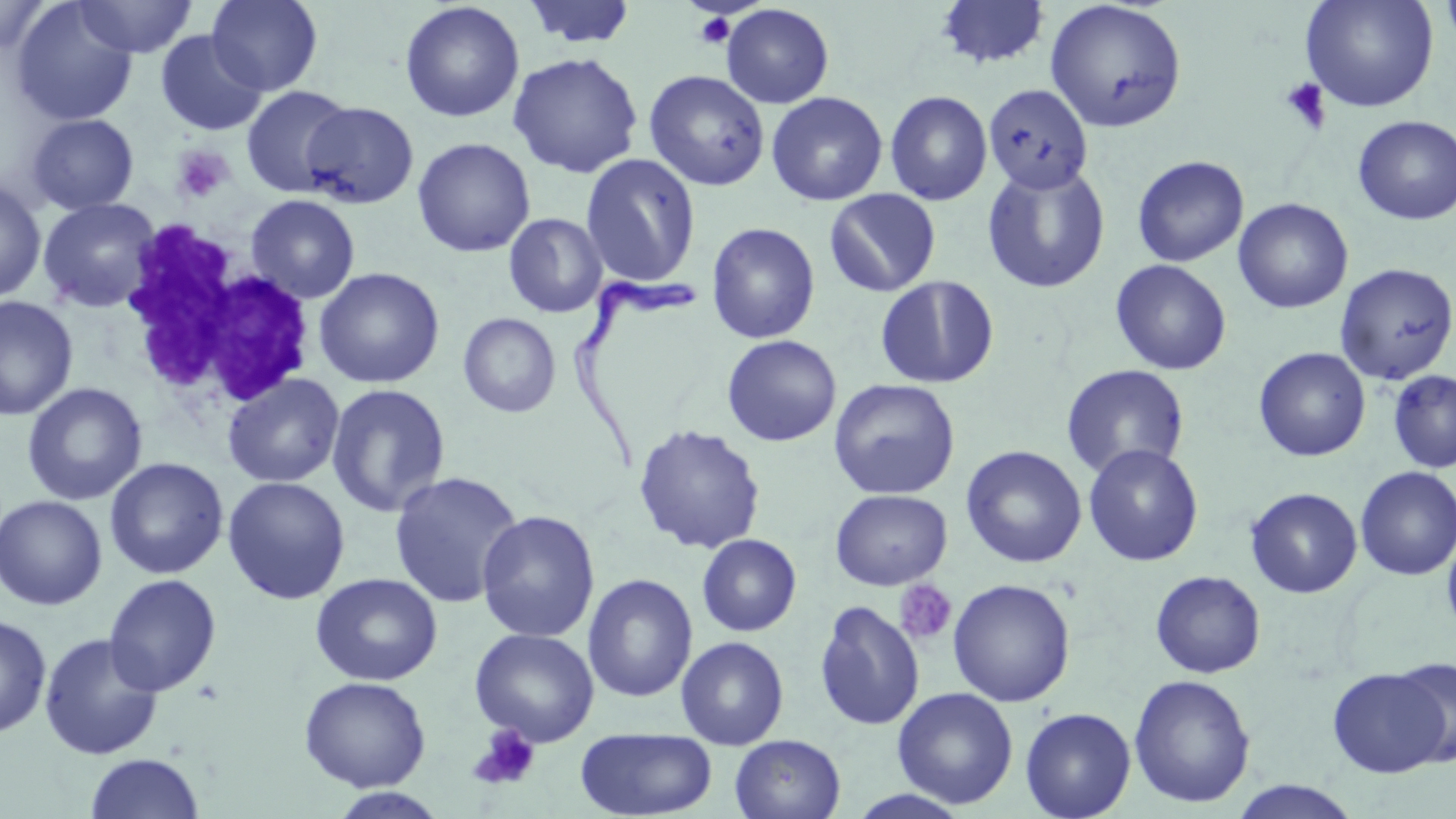
slide_level_diagnosis: Trypanosoma brucei
platelet_locations: 'approximate bounding boxes as (x1,y1)-(x2,y2) corner pairs in pixels: (692,12)-(735,51), (1280,77)-(1332,133), (171,144)-(234,205), (894,580)-(958,646), (469,724)-(541,791)'
white_blood_cell_locations: 'approximate bounding boxes as (x1,y1)-(x2,y2) corner pairs in pixels: (113,226)-(320,416)'
magnification: 1000x
preparation: thin blood film
stain: May-Grünwald-Giemsa
field_of_view: single
trypanosoma_brucei_locations: 'approximate bounding boxes as (x1,y1)-(x2,y2) corner pairs in pixels: (569,261)-(705,470)'
image_size: 1456×819 pixels
modality: light microscopy
uninfected_red_blood_cell_locations: 'approximate bounding boxes as (x1,y1)-(x2,y2) corner pairs in pixels: (72,0)-(198,58), (206,0)-(324,95), (523,0)-(637,49), (934,0)-(1051,70), (1300,0)-(1439,113), (1439,0)-(1456,52), (1,1)-(55,53), (1045,1)-(1188,133), (399,2)-(525,123), (11,3)-(138,126), (719,4)-(834,109), (155,30)-(268,136), (508,52)-(644,178), (644,70)-(770,191), (983,83)-(1094,194), (240,85)-(354,197), (884,90)-(993,206), (765,91)-(888,206), (300,101)-(419,209), (26,114)-(140,215), (1353,116)-(1456,225), (412,137)-(536,257), (580,154)-(701,289), (1133,155)-(1248,267), (981,163)-(1111,294), (0,178)-(47,304), (824,189)-(941,297), (245,194)-(360,304), (38,197)-(162,314), (1233,198)-(1353,314), (503,213)-(608,318), (706,222)-(820,343), (1110,259)-(1231,375), (1334,263)-(1456,385), (313,267)-(445,389), (875,275)-(1000,389), (0,296)-(79,421), (458,313)-(561,418), (722,335)-(841,447), (1253,346)-(1371,462), (1061,364)-(1189,480), (1387,369)-(1456,473), (222,373)-(345,488), (828,378)-(961,500), (22,382)-(147,506), (325,383)-(451,517), (633,424)-(766,554), (1083,443)-(1203,566), (961,445)-(1087,568), (104,457)-(229,579), (1355,466)-(1456,580), (388,470)-(524,609), (222,476)-(350,604), (1245,487)-(1362,598), (830,489)-(952,590), (0,494)-(107,610), (477,510)-(600,642), (1441,526)-(1456,639), (696,533)-(802,637), (1150,570)-(1266,678), (310,572)-(443,686), (103,573)-(222,697), (583,573)-(698,703), (948,578)-(1076,707), (814,601)-(925,730), (0,614)-(52,739), (469,627)-(599,747), (39,632)-(164,760), (676,636)-(789,750), (1391,656)-(1456,768), (1328,667)-(1449,777), (1128,674)-(1256,808), (298,675)-(431,792), (892,687)-(1018,808), (1020,707)-(1136,819), (575,727)-(718,818), (729,734)-(846,819), (84,752)-(204,818), (1227,780)-(1364,819), (327,788)-(450,818), (844,789)-(974,819)'